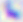

Summary:
  - Modality: photomicrograph
  - Identification: Toxoplasma gondii
  - Magnification: 400x